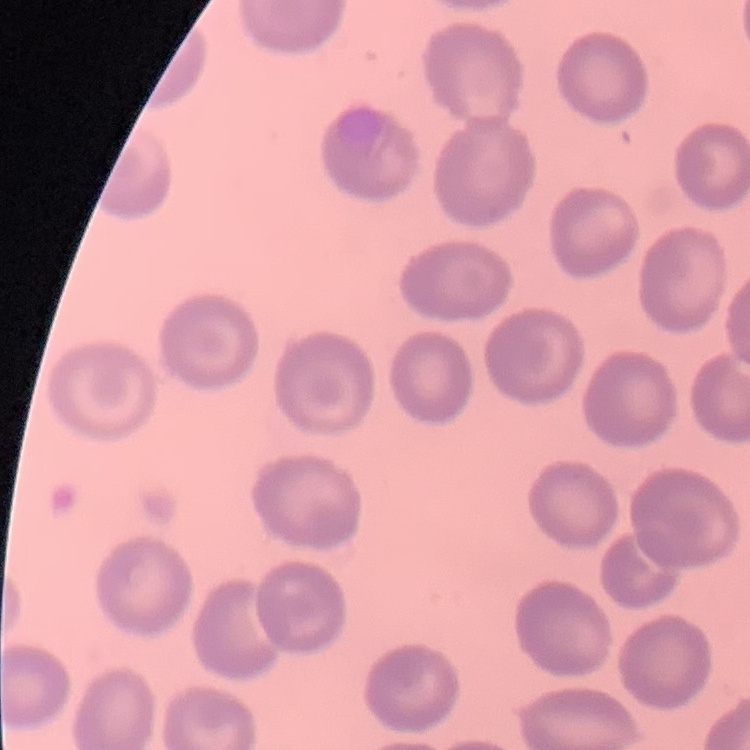 The erythrocytes show no rouleaux formation. Thin peripheral smear. Square crop of a larger photomicrograph. Stained with either Field's or Giemsa.